Identify the parasite.
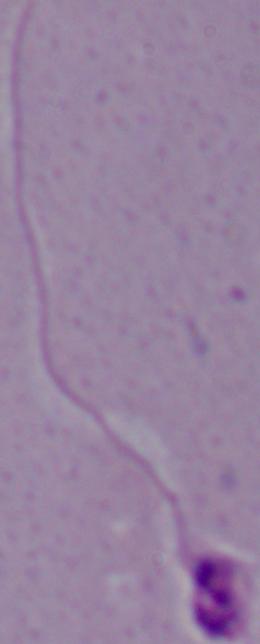

This is Leishmania.

Summary:
  - Magnification: 1000x
  - Modality: photomicrograph